Locate the Plasmodium falciparum-infected red blood cells and any of indeterminate infection status.
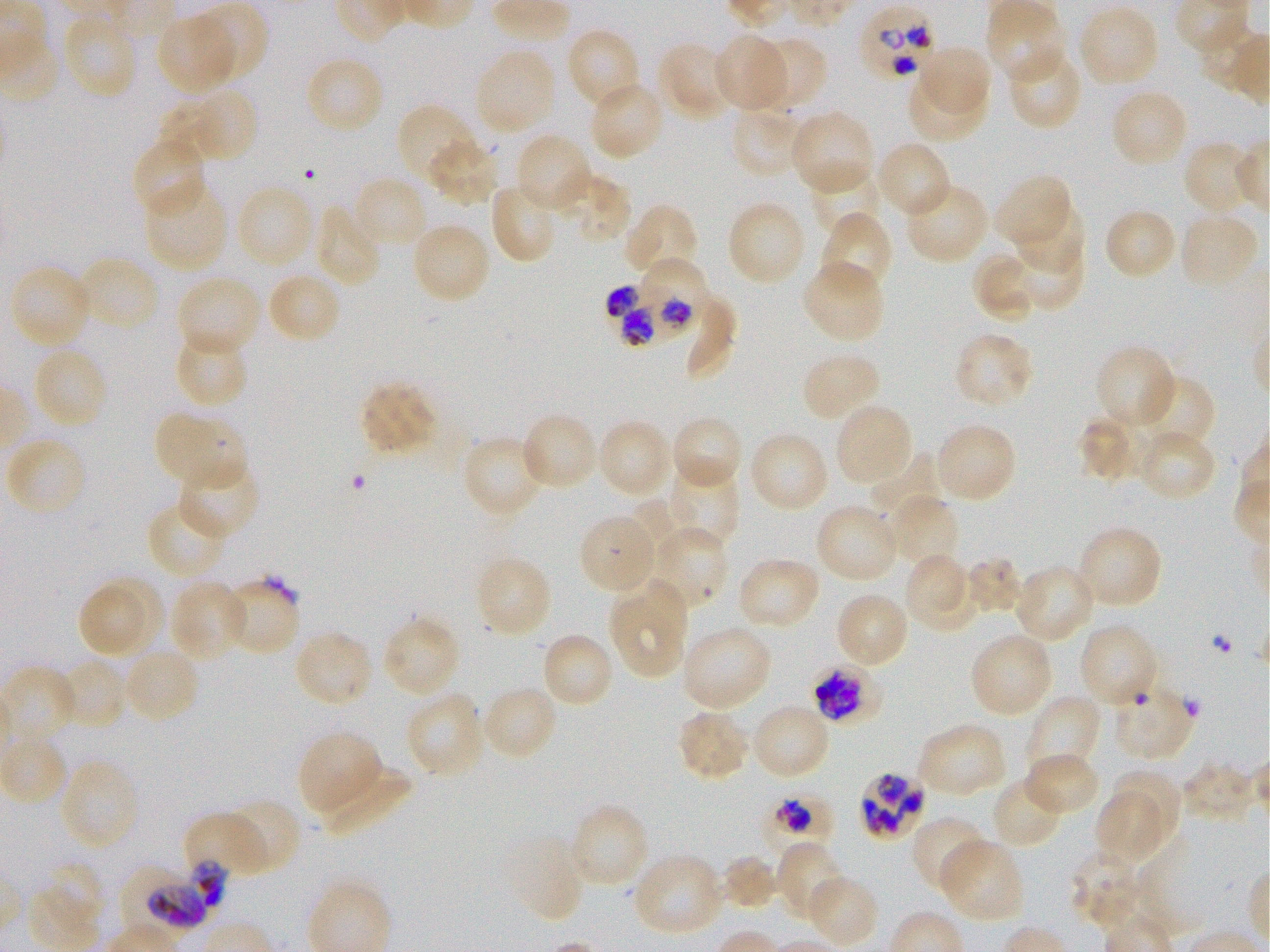

Approximate bounding boxes as [x1, y1, x2, y2] in pixels. Not every red blood cell is marked. A life-cycle stage — or a range of stages, where the recorded stages span more than one — follows each staged infected red blood cell.
Infected red blood cells: [858, 5, 942, 80]; [643, 257, 710, 330] early trophozoite; [609, 278, 689, 362]; [809, 659, 890, 732] early trophozoite to early schizont; [860, 771, 926, 839]; [759, 787, 838, 858] trophozoite; [118, 866, 206, 939] trophozoite.
Red blood cells of indeterminate infection status: [216, 577, 303, 656], [192, 856, 225, 912].

Summary:
  - Locations of uninfected red blood cells: [985, 0, 1066, 85], [187, 1, 269, 87], [1076, 4, 1161, 89], [60, 12, 138, 101], [155, 12, 238, 95], [1198, 24, 1268, 95], [566, 27, 643, 112], [713, 32, 790, 114], [757, 36, 827, 105], [657, 40, 739, 121], [917, 42, 997, 119], [1004, 44, 1084, 130], [473, 46, 557, 138], [303, 54, 385, 135], [908, 69, 986, 139], [588, 80, 667, 162], [1110, 87, 1190, 168], [189, 88, 258, 166], [395, 102, 484, 191], [729, 104, 808, 178], [789, 108, 876, 197], [513, 132, 595, 214], [131, 135, 208, 220], [425, 136, 499, 207], [874, 141, 953, 220], [1182, 141, 1262, 218], [807, 164, 881, 235], [550, 171, 630, 245], [993, 173, 1075, 253], [352, 175, 431, 250], [144, 179, 230, 274], [489, 180, 561, 264], [903, 181, 991, 264], [234, 184, 317, 270], [725, 199, 806, 288], [1009, 200, 1084, 277], [312, 203, 382, 289], [623, 203, 699, 281], [1102, 207, 1178, 281], [1178, 210, 1261, 291], [818, 211, 893, 298], [410, 221, 492, 305], [995, 237, 1084, 315], [973, 249, 1049, 321], [74, 256, 161, 335], [800, 260, 885, 345], [8, 263, 94, 350], [265, 271, 343, 345], [175, 275, 264, 357], [173, 330, 249, 409], [952, 331, 1034, 410], [31, 345, 109, 431], [1094, 345, 1178, 430], [801, 350, 883, 423], [1131, 374, 1216, 456], [359, 379, 439, 456], [832, 402, 915, 489], [152, 408, 249, 491], [519, 412, 600, 492], [669, 414, 743, 491], [1078, 415, 1153, 483], [596, 418, 674, 500], [933, 421, 1017, 504], [1133, 428, 1217, 502], [747, 429, 831, 513], [3, 435, 89, 519], [460, 435, 550, 520], [176, 458, 260, 541], [666, 459, 740, 549], [884, 494, 960, 571], [146, 500, 231, 580], [814, 502, 901, 584], [578, 513, 660, 596], [646, 523, 727, 613], [1075, 523, 1164, 610], [903, 552, 979, 634], [473, 554, 554, 640], [736, 555, 823, 631], [964, 557, 1023, 615], [1012, 563, 1096, 644], [76, 574, 164, 661], [169, 579, 249, 663], [608, 580, 690, 680], [832, 591, 911, 670], [380, 615, 461, 699], [1077, 622, 1161, 711], [680, 623, 773, 714], [292, 628, 374, 709], [968, 630, 1053, 719], [539, 631, 614, 710], [121, 646, 201, 724], [55, 657, 130, 728], [1109, 682, 1197, 762], [480, 684, 559, 763], [404, 691, 485, 779], [1024, 695, 1103, 780], [748, 702, 832, 781], [676, 709, 753, 782], [915, 722, 1008, 799], [296, 729, 383, 817], [0, 736, 69, 808], [1022, 751, 1102, 816], [313, 756, 408, 835], [57, 759, 139, 853], [1110, 766, 1187, 855], [991, 775, 1065, 850], [1097, 787, 1166, 863], [216, 798, 301, 875], [568, 802, 650, 891], [185, 811, 278, 874], [910, 814, 991, 895], [501, 833, 586, 923], [935, 837, 1024, 924], [775, 840, 848, 925], [1068, 848, 1148, 931], [631, 852, 727, 938], [719, 854, 778, 910], [37, 861, 104, 938], [804, 874, 879, 949]
  - Culture: in-vitro Plasmodium falciparum strain 3D7, static
  - Image size: 1270×952 pixels
  - Preparation: thin blood film
  - Field of view: single
  - Objective: 100x, oil immersion, numerical aperture 1.25
  - Donor blood group: O+
  - Stain: Giemsa